Locate every Plasmodium falciparum-infected red blood cell.
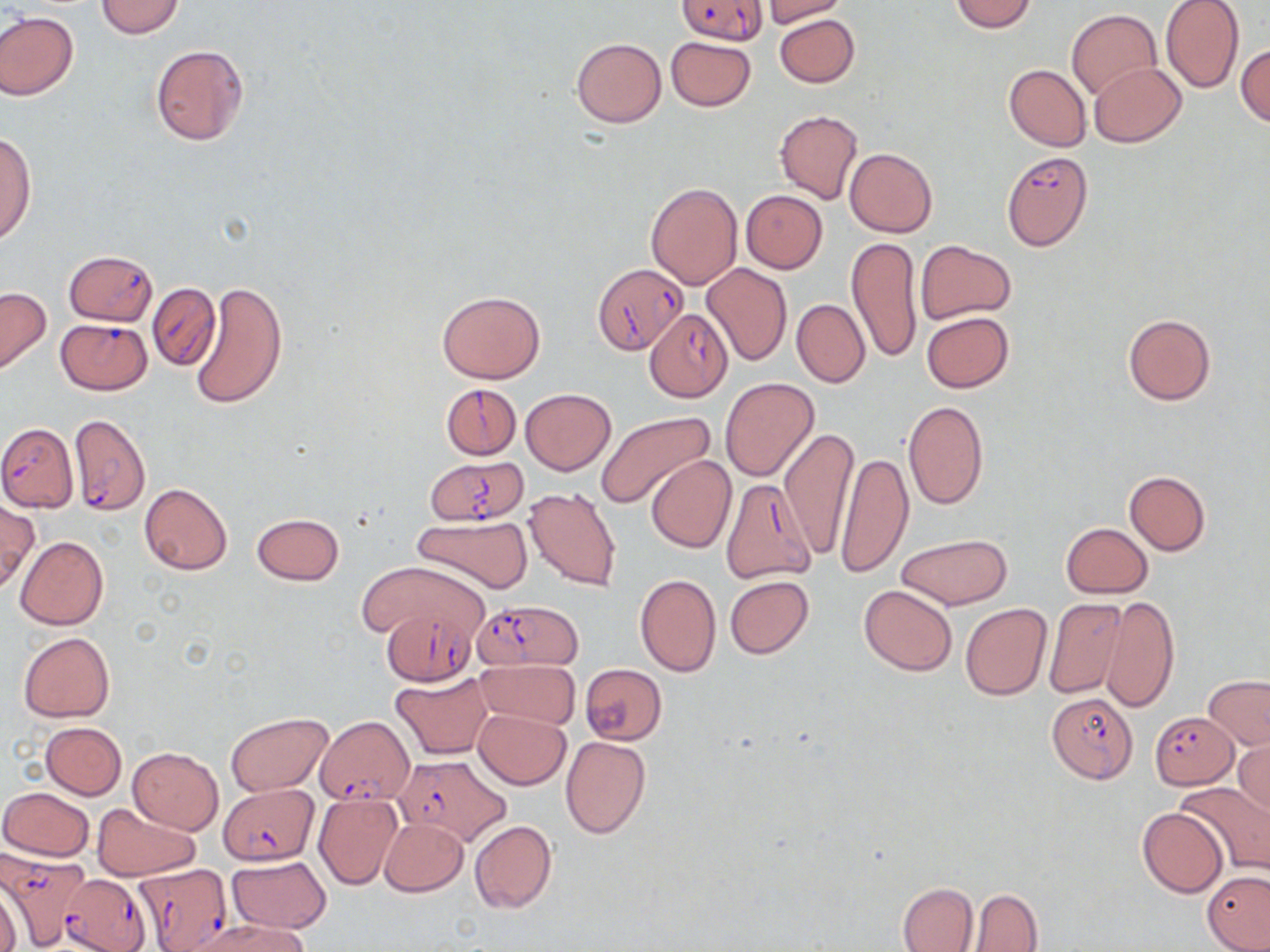

Approximate bounding boxes as [x1, y1, x2, y2] in pixels.
Plasmodium falciparum-infected red blood cells: [678, 0, 768, 44], [1000, 151, 1093, 252], [64, 249, 157, 325], [594, 262, 687, 352], [147, 283, 221, 371], [643, 308, 734, 402], [55, 318, 152, 395], [439, 382, 522, 461], [69, 412, 151, 517], [0, 423, 78, 511], [425, 457, 528, 526], [722, 478, 818, 584], [475, 599, 584, 670], [380, 608, 479, 686], [1045, 690, 1137, 784], [1150, 711, 1238, 789], [319, 717, 412, 804], [393, 755, 512, 845], [219, 784, 319, 865], [2, 854, 89, 951], [131, 864, 233, 952], [58, 873, 150, 952].

Uninfected red blood cell locations: [95, 0, 185, 38], [760, 0, 847, 25], [949, 0, 1038, 32], [1160, 1, 1245, 93], [1067, 9, 1162, 101], [0, 12, 79, 100], [774, 14, 859, 87], [665, 35, 756, 112], [571, 37, 666, 128], [150, 44, 248, 144], [1236, 44, 1270, 127], [1088, 62, 1186, 147], [1004, 64, 1091, 151], [774, 109, 863, 203], [1, 131, 35, 246], [845, 147, 937, 238], [646, 181, 742, 287], [741, 189, 827, 274], [848, 237, 923, 363], [914, 239, 1017, 324], [702, 261, 792, 366], [190, 280, 288, 410], [0, 287, 51, 375], [437, 291, 546, 384], [791, 299, 870, 388], [921, 311, 1014, 392], [1121, 312, 1217, 407], [720, 378, 819, 483], [521, 389, 615, 475], [903, 400, 989, 511], [594, 411, 714, 507], [779, 426, 857, 559], [835, 448, 914, 579], [646, 455, 737, 553], [1124, 470, 1211, 555], [139, 483, 231, 575], [522, 486, 621, 591], [0, 501, 38, 595], [251, 513, 344, 586], [412, 514, 533, 595], [1060, 523, 1153, 598], [895, 532, 1016, 609], [15, 535, 108, 629], [358, 561, 487, 644], [634, 573, 721, 677], [724, 576, 813, 659], [859, 584, 959, 675], [1043, 596, 1129, 698], [1099, 596, 1180, 714], [960, 603, 1052, 702], [19, 632, 114, 723], [476, 660, 579, 729], [580, 663, 667, 746], [392, 672, 492, 759], [1204, 675, 1270, 749], [473, 709, 571, 790], [225, 713, 332, 796], [40, 722, 127, 799], [561, 736, 652, 839], [1233, 738, 1270, 818], [127, 747, 224, 834], [1177, 782, 1270, 876], [2, 786, 93, 861], [312, 792, 402, 890], [92, 802, 201, 881], [1136, 808, 1226, 896], [379, 817, 468, 896], [469, 819, 557, 915], [227, 856, 331, 933], [1202, 870, 1270, 950], [897, 882, 978, 952], [970, 889, 1042, 951], [181, 917, 312, 952]. Slide-level diagnosis: Plasmodium falciparum. Single field of view. Thin blood smear. Captured at 1000x magnification. Image is 1270×952 pixels. Optical microscopy. May-Grünwald-Giemsa-stained preparation.